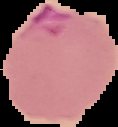

Image is 118×127 pixels. Cell region segmented out of the field of view; the surrounding area is masked to black. Result: malaria parasites identified. From a thin blood smear.